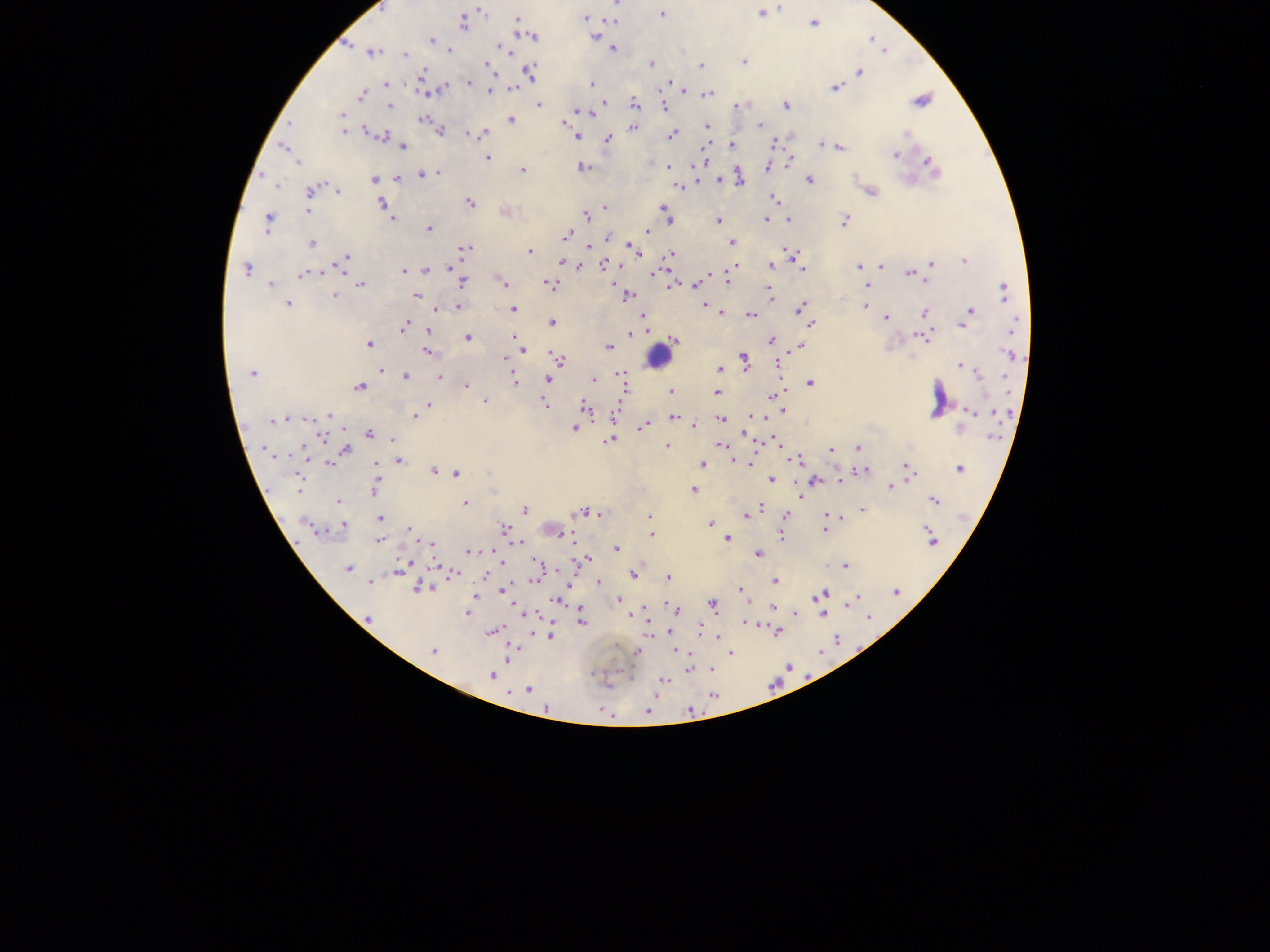

Approximate centers as [x, y] in pixels.
Summary:
  - Leukocyte locations: [657, 357]
  - Malaria parasite locations: [617, 4], [379, 7], [781, 7], [483, 11], [761, 13], [662, 14], [584, 18], [518, 19], [613, 21], [464, 22], [814, 23], [531, 36], [594, 36], [431, 41], [503, 48], [612, 49], [449, 50], [372, 52], [405, 54], [743, 62], [488, 65], [651, 65], [701, 66], [422, 72], [530, 72], [860, 72], [469, 82], [592, 83], [387, 84], [671, 84], [445, 87], [834, 87], [512, 89], [489, 91], [361, 95], [707, 95], [920, 101], [605, 103], [539, 105], [634, 105], [785, 105], [390, 106], [665, 106], [736, 106], [580, 111], [589, 113], [343, 116], [511, 119], [423, 120], [343, 124], [760, 125], [708, 126], [633, 128], [441, 130], [343, 131], [370, 132], [468, 133], [482, 133], [907, 134], [576, 135], [671, 135], [381, 136], [609, 139], [732, 144], [821, 145], [284, 147], [402, 147], [840, 147], [895, 156], [487, 158], [297, 162], [768, 166], [582, 167], [669, 167], [933, 167], [522, 170], [439, 173], [432, 174], [422, 175], [398, 178], [374, 180], [719, 180], [740, 180], [809, 180], [276, 186], [679, 186], [310, 191], [337, 192], [871, 192], [775, 199], [469, 203], [382, 204], [605, 207], [663, 208], [308, 211], [667, 214], [586, 215], [392, 218], [668, 220], [766, 220], [789, 220], [845, 220], [268, 221], [718, 221], [429, 228], [647, 231], [567, 235], [607, 238], [732, 242], [312, 243], [630, 244], [466, 248], [590, 248], [633, 249], [530, 252], [637, 253], [670, 254], [346, 258], [795, 258], [562, 261], [965, 261], [931, 264], [603, 265], [577, 266], [772, 266], [881, 266], [859, 267], [450, 268], [246, 270], [426, 270], [403, 271], [303, 274], [655, 274], [909, 274], [727, 278], [699, 281], [502, 282], [462, 283], [360, 284], [270, 285], [550, 285], [693, 285], [672, 286], [868, 287], [1004, 291], [770, 292], [415, 295], [628, 295], [335, 296], [288, 304], [704, 304], [865, 306], [459, 307], [801, 308], [435, 309], [513, 309], [970, 310], [925, 312], [721, 313], [752, 315], [642, 316], [885, 318], [966, 320], [552, 323], [1015, 324], [811, 325], [962, 326], [403, 328], [428, 330], [631, 333], [923, 337], [467, 338], [515, 338], [674, 340], [771, 340], [369, 344], [519, 344], [608, 347], [799, 347], [523, 350], [427, 352], [1009, 354], [558, 358], [506, 359], [745, 360], [961, 366], [380, 370], [720, 370], [253, 373], [620, 374], [979, 375], [405, 376], [439, 378], [549, 379], [594, 379], [622, 380], [514, 381], [810, 384], [467, 386], [359, 387], [671, 391], [717, 394], [772, 396], [485, 401], [429, 404], [545, 404], [585, 407], [782, 411], [971, 411], [615, 414], [330, 415], [754, 416], [414, 417], [674, 417], [309, 418], [288, 419], [722, 419], [280, 420], [272, 422], [694, 424], [574, 428], [642, 428], [959, 428], [370, 433], [993, 436], [323, 437], [393, 439], [609, 441], [719, 444], [668, 447], [858, 447], [263, 450], [345, 450], [832, 450], [798, 460], [399, 461], [739, 461], [330, 463], [747, 463], [702, 464], [908, 468], [960, 468], [434, 471], [863, 471], [457, 473], [772, 479], [813, 480], [840, 480], [300, 483], [891, 487], [375, 489], [694, 490], [934, 500], [338, 501], [465, 503], [761, 506], [757, 509], [524, 510], [862, 510], [582, 512], [746, 514], [785, 515], [650, 516], [379, 517], [710, 524], [343, 525], [504, 528], [824, 529], [408, 530], [652, 535], [782, 535], [565, 536], [727, 539], [931, 540], [378, 541], [518, 542], [430, 543], [616, 548], [470, 551], [758, 555], [582, 560], [540, 566], [844, 566], [347, 568], [398, 570], [453, 573], [633, 575], [485, 577], [537, 577], [668, 578], [775, 580], [369, 582], [599, 582], [420, 587], [741, 589], [503, 590], [895, 592], [743, 593], [822, 595], [475, 598], [857, 598], [558, 600], [619, 600], [851, 603], [713, 604], [774, 608], [675, 610], [467, 613], [796, 613], [822, 614], [368, 618], [582, 622], [747, 622], [491, 632], [777, 632], [551, 635], [718, 637], [432, 651], [677, 651], [637, 652], [731, 654], [507, 657], [689, 669], [491, 675], [663, 681], [528, 689], [713, 696], [647, 712]
  - Image size: 1270×952 pixels
  - Country: Ghana
  - Preparation: thick blood film
  - Capture: mobile-phone photograph through a microscope
  - Field of view: single